State which parasite is depicted.
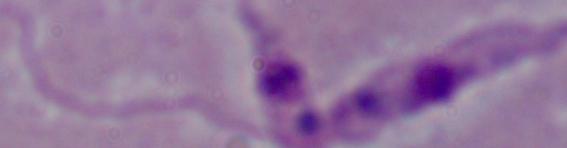

Leishmania.

Photomicrograph. 1000x magnification.